Describe the morphology of the red blood cells.
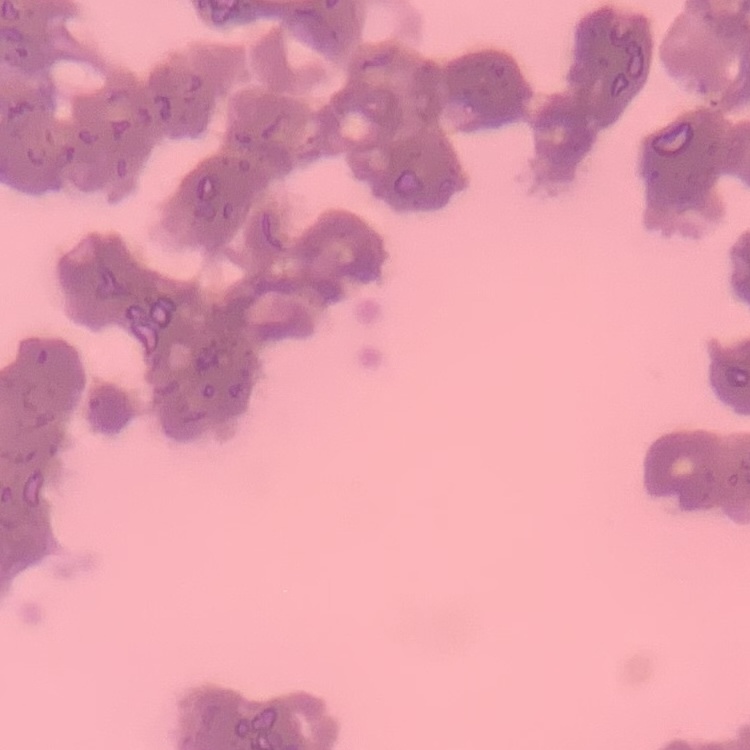

They show rouleaux formation.

One tile cut from a larger photomicrograph. Thin peripheral smear. Stained with either Field's or Giemsa.